State the blood parasite species.
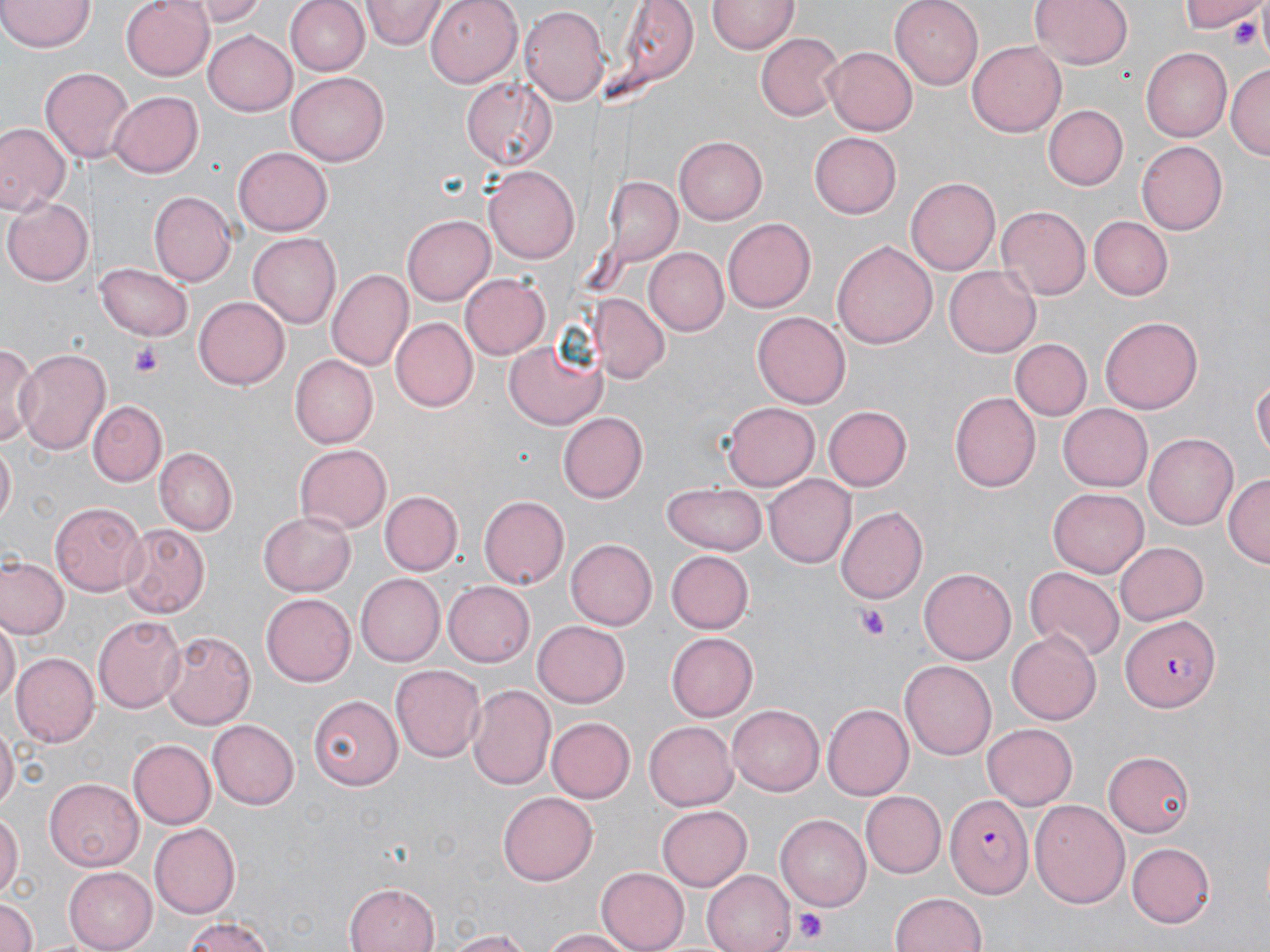

Plasmodium falciparum.

Summary:
  - Coordinate format: approximate bounding boxes as (x1,y1)-(x2,y2) corner pairs in pixels
  - Platelet locations: (1228,9)-(1268,51), (132,343)-(165,376), (856,606)-(891,640), (795,908)-(829,944)
  - Uninfected red blood cell locations: (0,0)-(94,53), (121,0)-(214,80), (192,0)-(268,25), (285,0)-(367,76), (363,0)-(443,51), (423,0)-(523,88), (615,0)-(700,91), (892,0)-(983,89), (1028,0)-(1137,72), (1184,0)-(1268,38), (708,1)-(797,57), (519,7)-(609,107), (203,31)-(298,115), (755,31)-(845,122), (968,40)-(1065,137), (822,46)-(916,134), (1141,48)-(1231,141), (1226,61)-(1269,158), (40,65)-(133,165), (286,71)-(390,168), (462,76)-(558,170), (108,91)-(204,177), (1043,104)-(1128,190), (0,123)-(67,216), (810,133)-(902,217), (676,136)-(766,224), (1136,140)-(1226,235), (232,145)-(331,234), (484,166)-(579,265), (601,176)-(682,269), (908,176)-(1003,275), (151,191)-(236,286), (3,197)-(93,287), (998,205)-(1091,299), (403,214)-(496,306), (722,217)-(816,313), (1089,217)-(1173,299), (248,232)-(340,331), (832,239)-(938,351), (645,248)-(729,336), (95,264)-(196,340), (945,265)-(1039,357), (327,268)-(415,373), (459,273)-(550,361), (193,295)-(291,390), (590,295)-(669,384), (753,311)-(849,410), (1101,314)-(1201,410), (391,317)-(477,410), (1011,338)-(1092,420), (0,340)-(39,448), (505,341)-(607,430), (15,347)-(113,457), (292,355)-(378,449), (1252,374)-(1269,469), (949,392)-(1038,492), (88,401)-(168,487), (723,403)-(818,490), (1058,403)-(1152,490), (824,406)-(911,490), (558,413)-(648,502), (1146,432)-(1241,529), (0,445)-(16,530), (294,445)-(391,533), (155,448)-(237,534), (1225,472)-(1269,569), (765,476)-(855,567), (663,482)-(767,555), (1051,487)-(1148,576), (378,490)-(462,575), (479,497)-(568,589), (51,501)-(147,597), (835,506)-(927,604), (258,509)-(355,596), (119,522)-(211,616), (565,538)-(656,630), (1114,541)-(1209,625), (666,551)-(754,633), (2,557)-(67,640), (919,567)-(1015,663), (1026,569)-(1121,659), (356,573)-(445,665), (444,580)-(536,667), (262,594)-(356,686), (92,615)-(185,713), (0,617)-(18,713), (533,621)-(629,707), (1007,627)-(1102,726), (160,629)-(257,730), (665,632)-(756,721), (12,652)-(98,746), (391,662)-(484,759), (900,662)-(995,759), (466,683)-(556,790), (309,695)-(402,788), (729,703)-(824,795), (821,704)-(912,801), (547,716)-(636,803), (208,718)-(301,809), (645,722)-(737,810), (982,722)-(1078,808), (0,725)-(17,814), (128,738)-(215,829), (1104,752)-(1196,836), (42,778)-(143,871), (499,790)-(596,882), (861,791)-(946,877), (1029,799)-(1129,908), (658,804)-(751,890), (0,811)-(22,901), (776,814)-(873,910), (150,823)-(241,917), (1126,842)-(1216,928), (65,865)-(159,952), (595,867)-(689,952), (703,869)-(799,952), (345,882)-(441,952), (890,891)-(988,952), (0,896)-(39,952), (180,916)-(281,952), (539,929)-(640,951), (441,930)-(536,951)
  - Plasmodium falciparum-infected red blood cell locations: (1121,616)-(1216,712), (946,794)-(1033,900)
  - Preparation: thin blood film
  - Image size: 1270×952 pixels
  - Modality: light microscopy
  - Stain: May-Grünwald-Giemsa
  - Magnification: 1000x
  - Field of view: single